Comment on the morphology of the red blood cells.
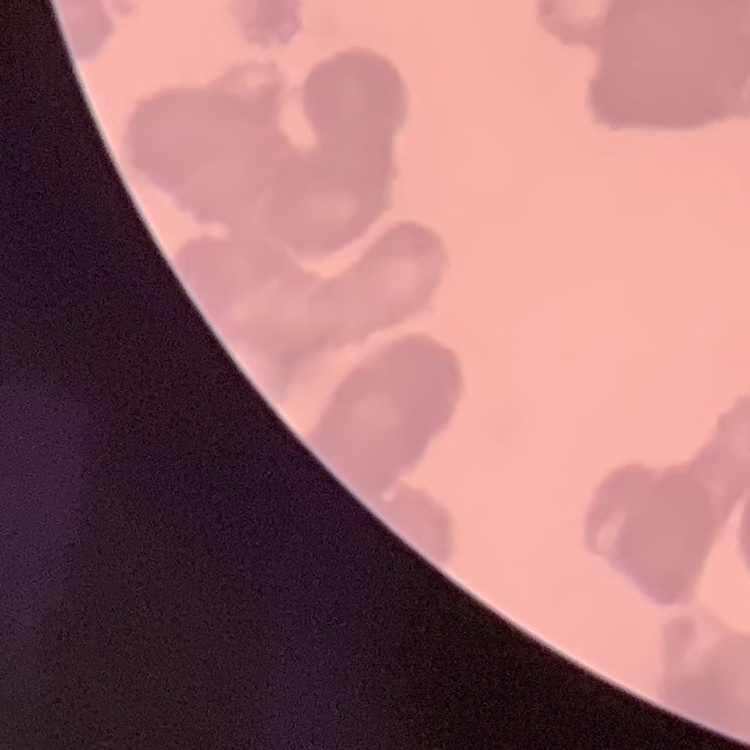
Rouleaux formation.

Summary:
  - Stain: Field's or Giemsa
  - Preparation: thin peripheral smear
  - Image type: one tile cut from a larger photomicrograph